Outline each Trypanosoma brucei.
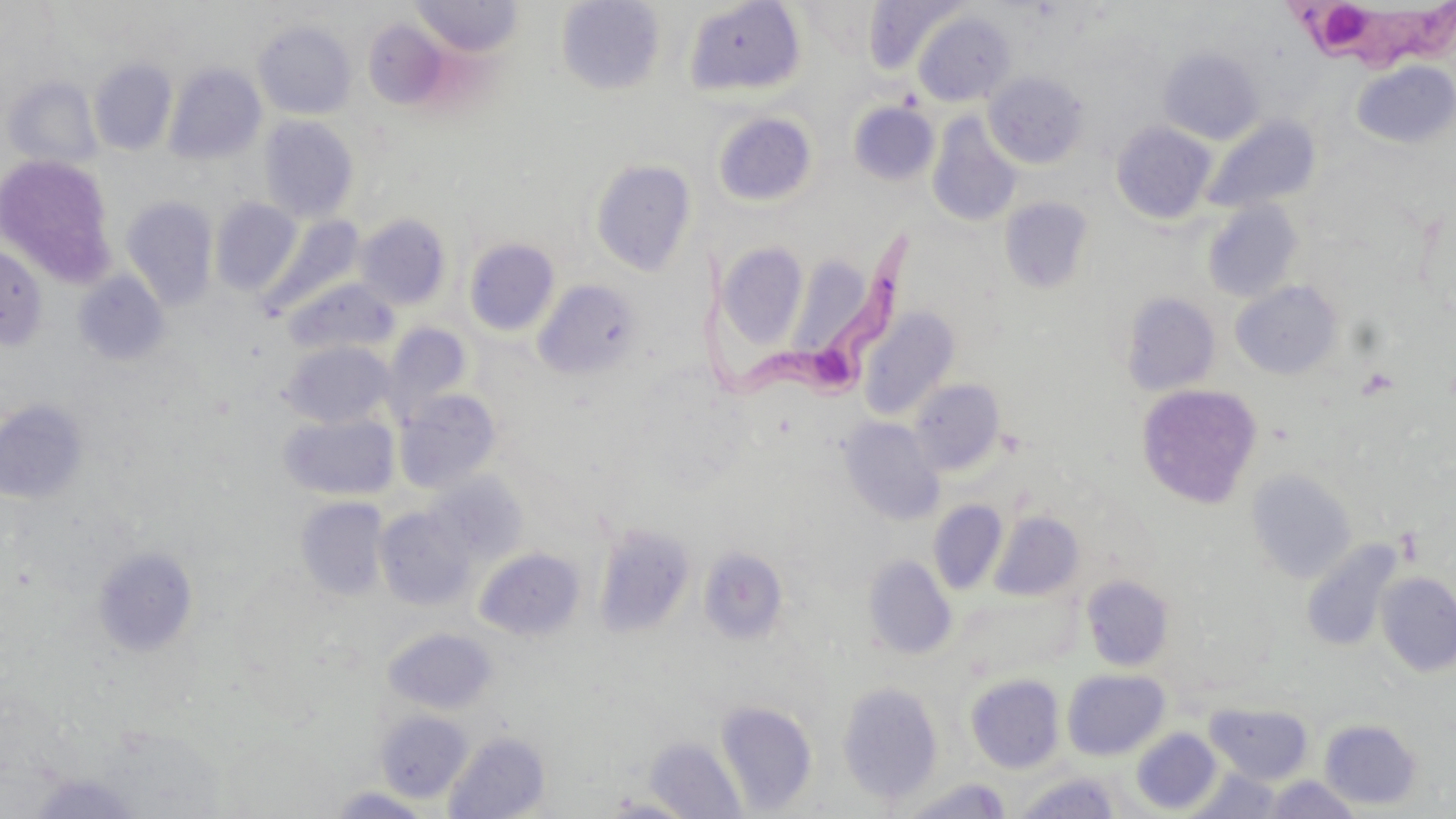

Approximate bounding boxes as [x1, y1, x2, y2] in pixels.
Trypanosoma brucei: [1283, 3, 1456, 75], [680, 237, 920, 400].

Platelet locations: [1356, 366, 1401, 400], [1394, 526, 1423, 565]. Uninfected red blood cell locations: [410, 0, 523, 58], [556, 0, 666, 95], [863, 0, 966, 76], [684, 1, 806, 97], [911, 10, 1016, 107], [253, 20, 356, 119], [364, 21, 450, 110], [1159, 48, 1264, 145], [89, 59, 177, 155], [1351, 60, 1456, 149], [164, 63, 266, 165], [984, 71, 1089, 169], [4, 76, 102, 171], [849, 102, 939, 186], [712, 111, 817, 207], [926, 112, 1023, 228], [259, 115, 360, 222], [1201, 116, 1320, 215], [1111, 121, 1217, 224], [1, 154, 117, 287], [590, 159, 697, 275], [121, 196, 218, 310], [1001, 197, 1094, 293], [210, 198, 302, 296], [1202, 201, 1302, 304], [355, 214, 451, 310], [261, 215, 365, 316], [464, 238, 559, 336], [716, 242, 808, 351], [0, 244, 47, 350], [787, 252, 882, 359], [74, 270, 169, 365], [284, 278, 399, 357], [533, 280, 642, 379], [1230, 281, 1343, 380], [1120, 291, 1220, 396], [860, 307, 960, 420], [383, 322, 473, 419], [280, 340, 396, 428], [909, 379, 1005, 475], [1137, 384, 1261, 509], [395, 389, 502, 493], [0, 399, 88, 504], [279, 413, 399, 500], [839, 417, 945, 526], [1246, 469, 1357, 584], [427, 473, 525, 563], [296, 496, 389, 600], [929, 501, 1008, 595], [375, 507, 474, 609], [990, 510, 1085, 601], [594, 523, 695, 639], [1301, 539, 1402, 652], [699, 546, 789, 644], [93, 547, 200, 656], [475, 547, 585, 640], [863, 555, 957, 659], [1376, 571, 1456, 677], [1081, 574, 1174, 671], [384, 627, 497, 715], [1062, 668, 1169, 759], [965, 673, 1064, 773], [836, 680, 944, 806], [716, 700, 817, 815], [1205, 702, 1313, 783], [375, 709, 473, 802], [1320, 719, 1422, 810], [1131, 728, 1220, 814], [444, 730, 550, 819], [643, 736, 746, 819], [1187, 767, 1285, 818], [26, 772, 144, 817], [1013, 772, 1123, 818], [1263, 775, 1363, 818], [895, 778, 1014, 818], [326, 786, 435, 818], [596, 795, 699, 818]. Slide-level diagnosis: Trypanosoma brucei. Single field of view. Image is 1456×819 pixels. Light microscopy. 1000x magnification. Thin blood smear. May-Grünwald-Giemsa-stained preparation.